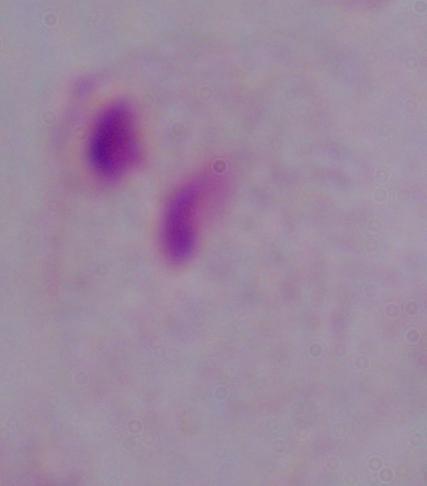
{
  "modality": "micrograph",
  "identification": "trichomonad",
  "magnification": "1000x"
}